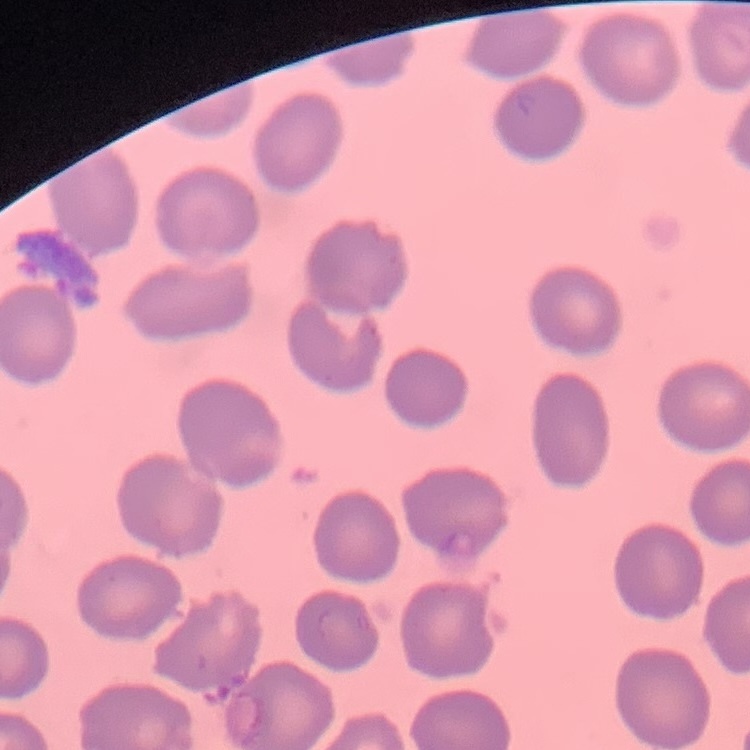
The erythrocytes exhibit no rouleaux formation. Thin blood film. Stained with either Field's or Giemsa. Square crop of a larger photomicrograph.